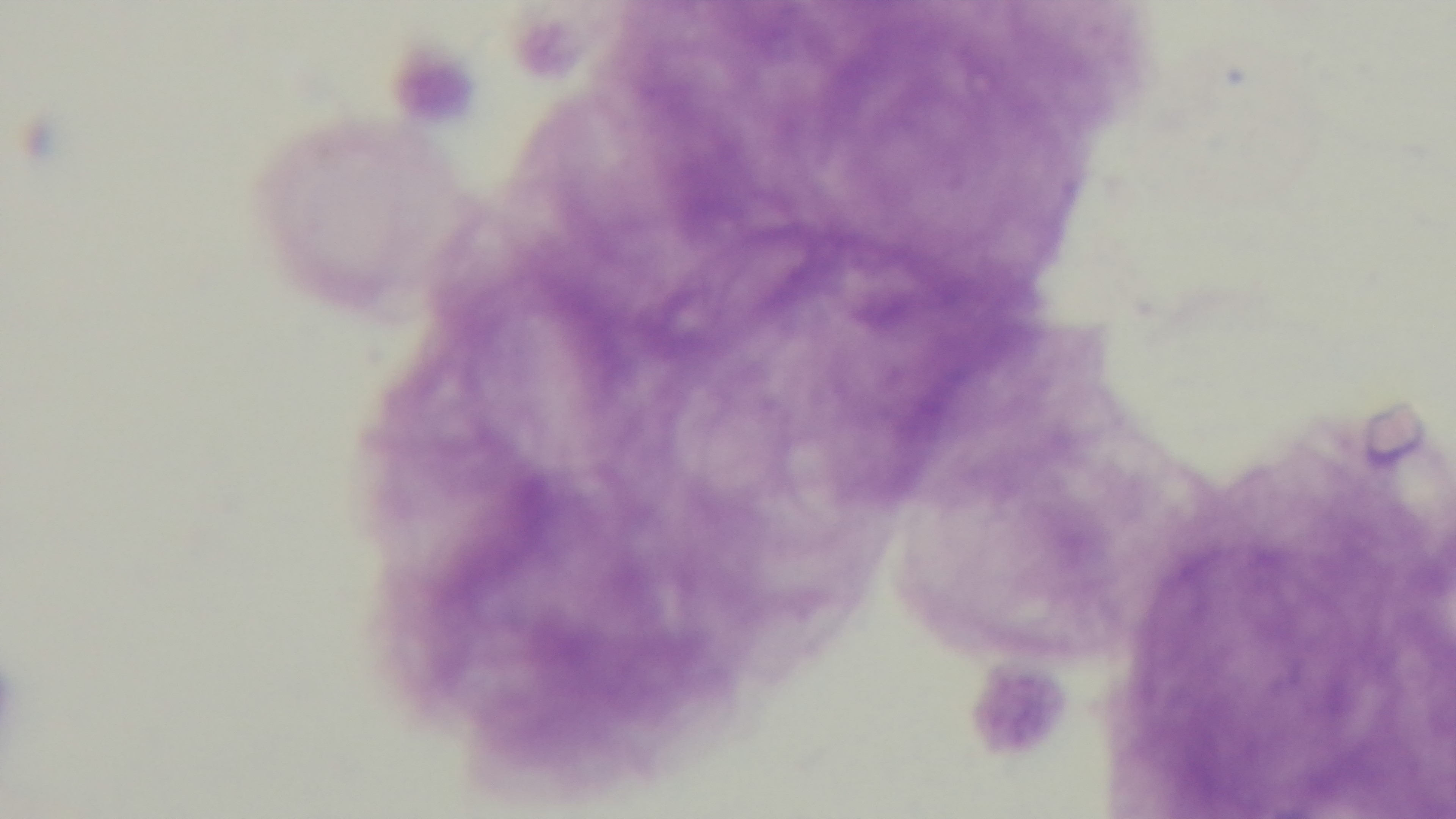 Preparation: thick blood film. Malaria status: negative. Giemsa-stained. Single field of view. 100x oil-immersion objective. Light microscopy. Captured with a mounted 4K digital camera.